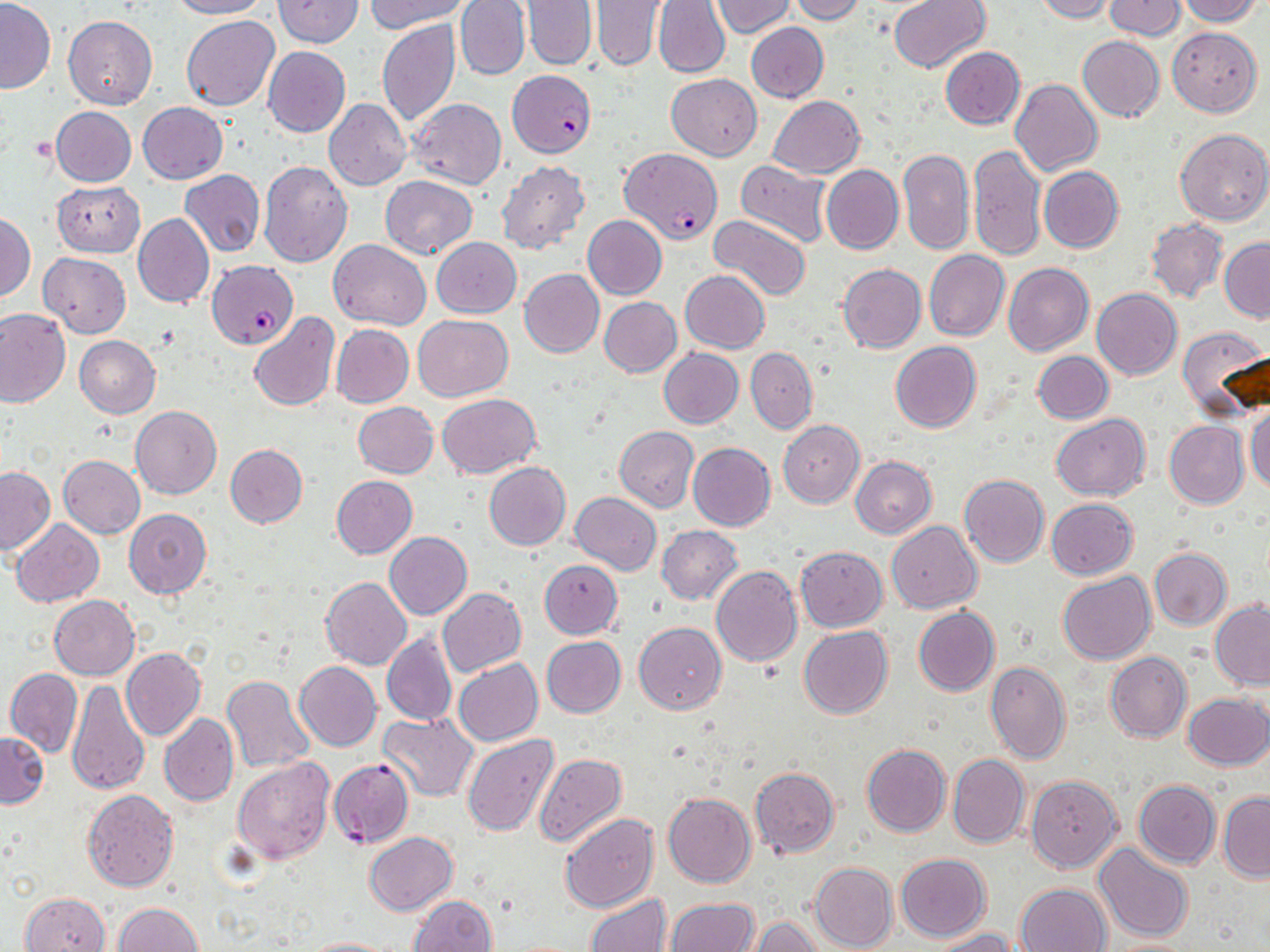

slide-level diagnosis = Plasmodium falciparum
uninfected red blood cell locations = approximate bounding boxes as [x1, y1, x2, y2] in pixels: [168, 0, 269, 20], [274, 0, 362, 48], [366, 0, 468, 33], [455, 0, 530, 81], [522, 0, 596, 69], [890, 0, 990, 73], [1033, 0, 1116, 22], [1104, 0, 1187, 40], [1174, 0, 1261, 25], [1, 1, 54, 93], [591, 1, 666, 70], [653, 1, 730, 77], [712, 1, 794, 38], [791, 1, 866, 24], [181, 15, 280, 110], [63, 16, 157, 109], [376, 19, 460, 127], [746, 22, 828, 103], [1167, 27, 1262, 115], [1077, 35, 1164, 121], [263, 45, 350, 137], [940, 47, 1024, 129], [666, 73, 762, 159], [1010, 79, 1103, 176], [769, 95, 865, 178], [406, 98, 507, 189], [324, 99, 411, 190], [138, 101, 227, 184], [50, 107, 136, 187], [1175, 128, 1270, 225], [969, 145, 1046, 260], [898, 148, 975, 255], [734, 159, 832, 247], [259, 160, 353, 267], [496, 161, 590, 255], [822, 165, 903, 255], [1039, 167, 1123, 253], [180, 169, 265, 257], [380, 175, 478, 259], [53, 181, 145, 256], [1, 213, 35, 301], [133, 213, 214, 308], [582, 215, 667, 301], [708, 215, 812, 302], [1146, 218, 1227, 303], [431, 237, 522, 317], [1220, 238, 1270, 321], [327, 239, 432, 328], [923, 250, 1009, 341], [39, 252, 131, 337], [837, 263, 926, 353], [1003, 263, 1095, 356], [519, 269, 604, 358], [680, 271, 770, 353], [1092, 288, 1182, 380], [599, 297, 681, 377], [0, 309, 70, 407], [248, 313, 339, 411], [413, 314, 513, 401], [331, 324, 414, 408], [1177, 325, 1270, 421], [74, 335, 161, 418], [890, 342, 982, 433], [659, 348, 744, 428], [746, 348, 817, 433], [1033, 351, 1114, 423], [437, 393, 540, 478], [353, 402, 438, 478], [1246, 404, 1270, 497], [131, 406, 222, 499], [1051, 413, 1149, 500], [779, 420, 865, 508], [1164, 421, 1248, 508], [614, 426, 699, 512], [688, 443, 776, 531], [225, 444, 307, 528], [59, 455, 145, 539], [851, 456, 936, 538], [484, 461, 571, 550], [0, 467, 55, 557], [959, 474, 1049, 567], [331, 475, 417, 558], [569, 493, 661, 576], [1046, 498, 1137, 579], [124, 508, 212, 599], [11, 519, 104, 606], [886, 522, 981, 613], [657, 526, 743, 605], [385, 532, 472, 620], [795, 546, 887, 631], [1149, 547, 1231, 630], [539, 560, 622, 638], [711, 565, 801, 667], [1057, 571, 1156, 664], [320, 577, 412, 669], [437, 588, 526, 676], [49, 596, 139, 679], [1210, 600, 1270, 689], [913, 606, 999, 696], [634, 622, 726, 715], [798, 626, 893, 719], [382, 630, 457, 726], [540, 637, 626, 718], [121, 647, 206, 740], [1104, 651, 1191, 743], [454, 658, 543, 747], [294, 661, 382, 751], [984, 661, 1071, 765], [4, 667, 83, 757], [221, 675, 314, 773], [65, 676, 149, 796], [1183, 692, 1270, 769], [159, 712, 238, 806], [378, 712, 479, 802], [0, 731, 48, 808], [463, 734, 559, 836], [862, 743, 951, 837], [534, 751, 626, 848], [948, 753, 1029, 848], [232, 757, 335, 865], [749, 767, 840, 857], [1025, 774, 1121, 872], [1134, 780, 1221, 867], [82, 789, 179, 892], [1218, 791, 1270, 883], [663, 792, 755, 887], [559, 813, 658, 913], [365, 832, 457, 914], [1093, 844, 1193, 943], [896, 853, 990, 941], [810, 862, 897, 952], [1016, 882, 1112, 952], [19, 891, 110, 952], [584, 893, 673, 952], [408, 895, 497, 952], [663, 899, 758, 952], [114, 902, 203, 952], [750, 917, 827, 952], [929, 929, 1017, 952], [298, 936, 395, 952], [1102, 939, 1201, 952]
Plasmodium falciparum-infected red blood cell locations = approximate bounding boxes as [x1, y1, x2, y2] in pixels: [506, 69, 597, 157], [620, 148, 721, 245], [207, 261, 298, 349], [329, 759, 415, 849]
preparation = thin blood film
modality = optical microscopy
field of view = single
magnification = 1000x
image size = 1270×952 pixels
stain = May-Grünwald-Giemsa